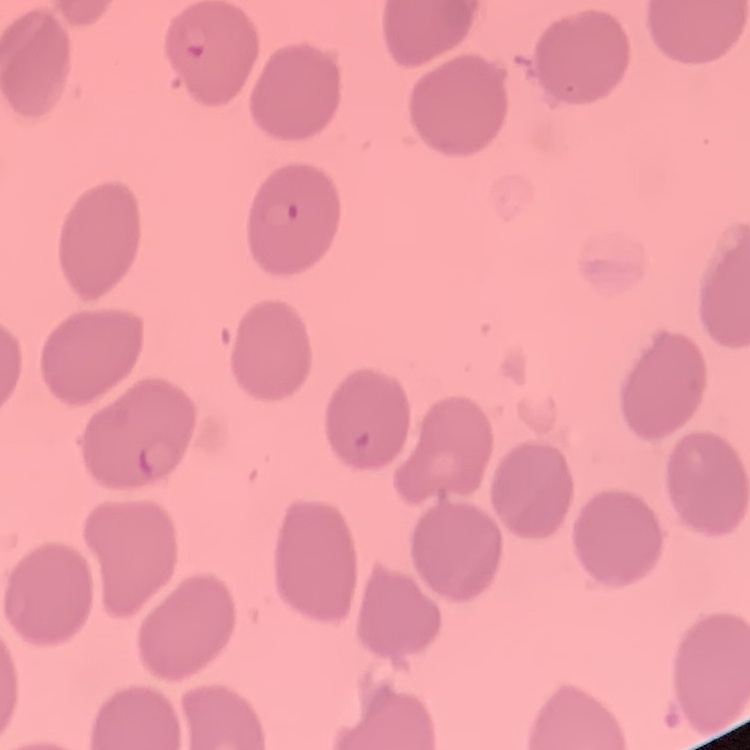
Summary:
  - Erythrocyte morphology: no rouleaux formation
  - Stain: Field's or Giemsa
  - Image type: one tile cut from a larger photomicrograph
  - Preparation: thin peripheral smear